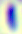

Summary:
  - Magnification: 400x
  - Identification: Toxoplasma gondii
  - Modality: photomicrograph